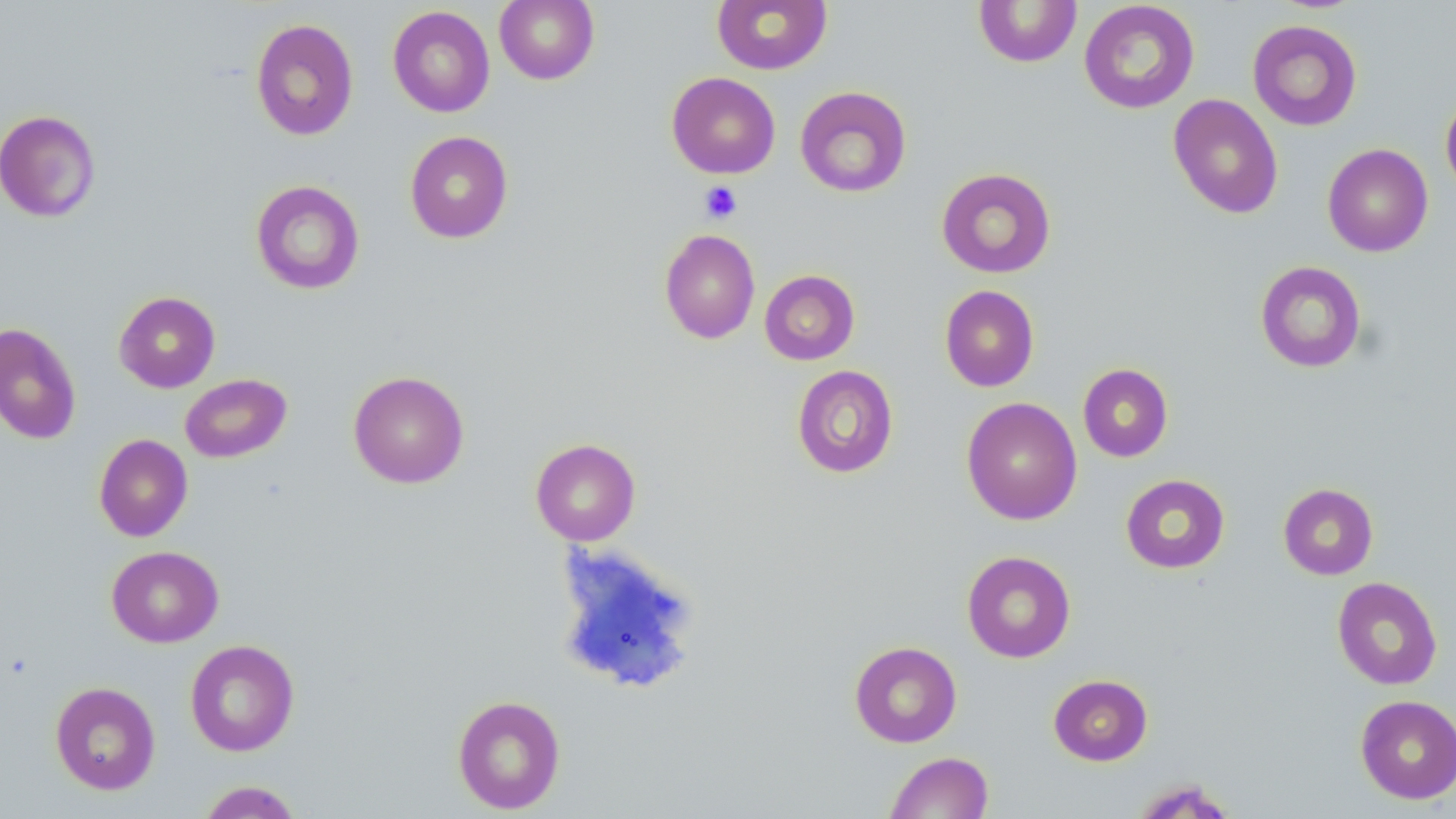

slide-level diagnosis = no evidence of blood parasites
magnification = 1000x
stain = May-Grünwald-Giemsa
modality = optical microscopy
image size = 1456×819 pixels
preparation = thin blood film
field of view = one of a larger specimen
uninfected red blood cell locations = approximate bounding boxes as [x1, y1, x2, y2] in pixels: [494, 0, 600, 85], [712, 0, 832, 74], [973, 1, 1082, 67], [1078, 1, 1200, 114], [387, 6, 495, 117], [250, 18, 359, 141], [1247, 19, 1362, 131], [666, 72, 780, 178], [795, 86, 912, 198], [1168, 93, 1284, 218], [1440, 95, 1456, 198], [0, 109, 101, 223], [404, 131, 513, 244], [1322, 143, 1433, 257], [936, 167, 1057, 278], [250, 180, 365, 295], [659, 229, 760, 344], [1254, 260, 1367, 373], [759, 269, 860, 365], [939, 285, 1039, 392], [114, 291, 221, 393], [0, 322, 82, 445], [1077, 363, 1173, 462], [791, 365, 898, 479], [348, 370, 470, 489], [180, 373, 292, 463], [961, 397, 1082, 525], [94, 434, 192, 542], [530, 438, 641, 546], [1120, 473, 1230, 574], [1278, 482, 1378, 580], [106, 545, 224, 648], [961, 550, 1076, 663], [1332, 576, 1442, 690], [185, 639, 299, 756], [849, 641, 962, 747], [1048, 674, 1153, 766], [50, 681, 161, 796], [452, 694, 566, 815], [1355, 695, 1456, 804], [885, 751, 994, 818], [1129, 778, 1239, 818], [196, 780, 304, 818]
platelet locations = approximate bounding boxes as [x1, y1, x2, y2] in pixels: [699, 181, 742, 223]